Identify the preparation type.
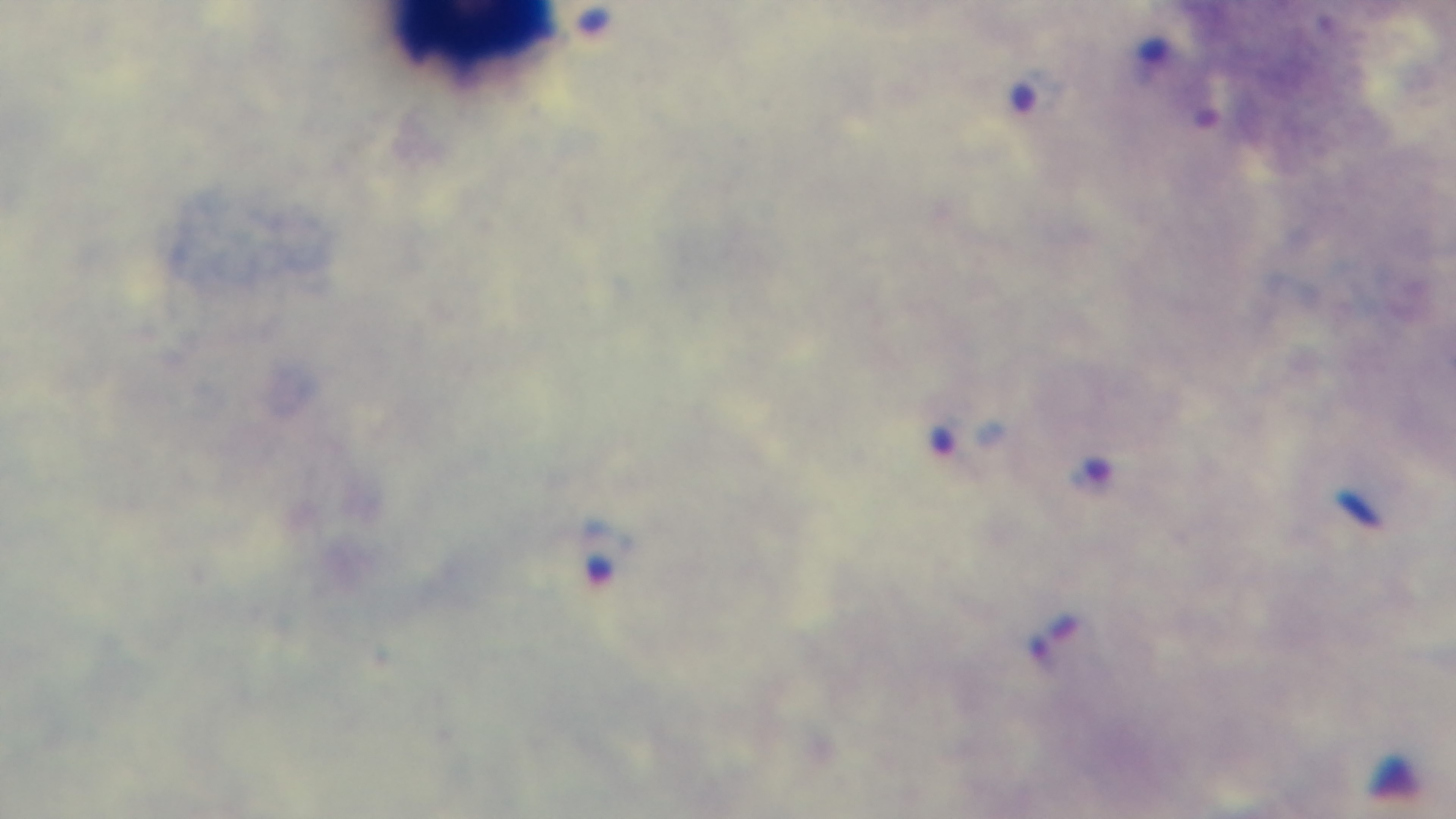
Thick.

Summary:
  - Malaria status: positive
  - Modality: light microscopy
  - Objective: 100x oil immersion
  - Field of view: one from the slide
  - Stain: Giemsa
  - Capture: mounted 4K digital camera